Describe the morphology of the red blood cells.
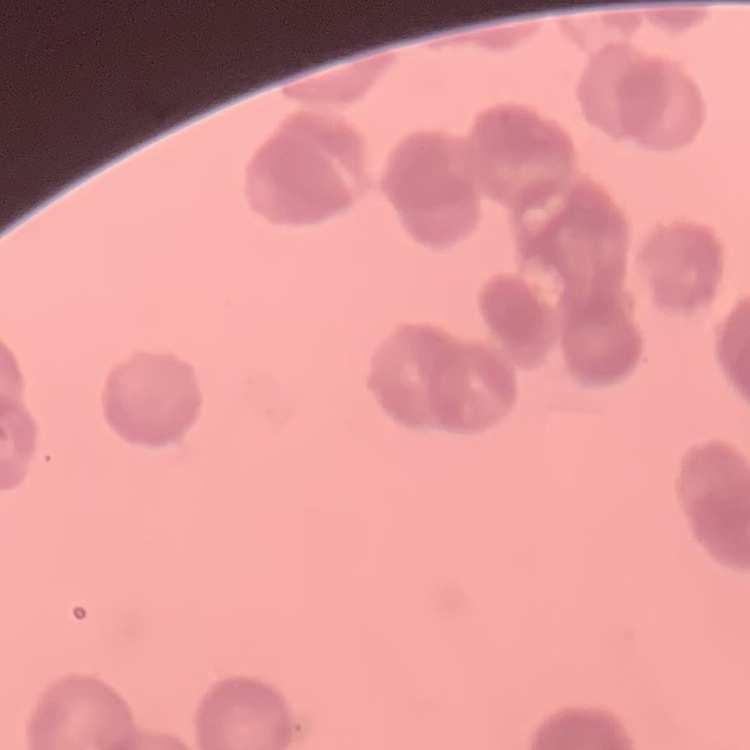

Rouleaux formation.

Summary:
  - Image type: square crop of a larger photomicrograph
  - Stain: Field's or Giemsa
  - Preparation: thin blood smear